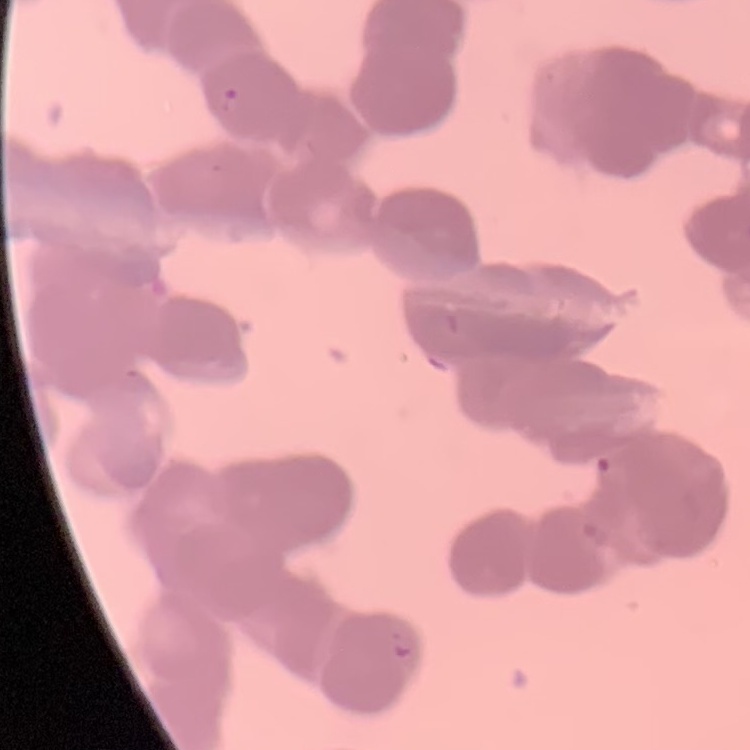

red blood cell morphology = rouleaux formation
preparation = thin blood film
stain = Field's or Giemsa
image type = square crop of a larger photomicrograph